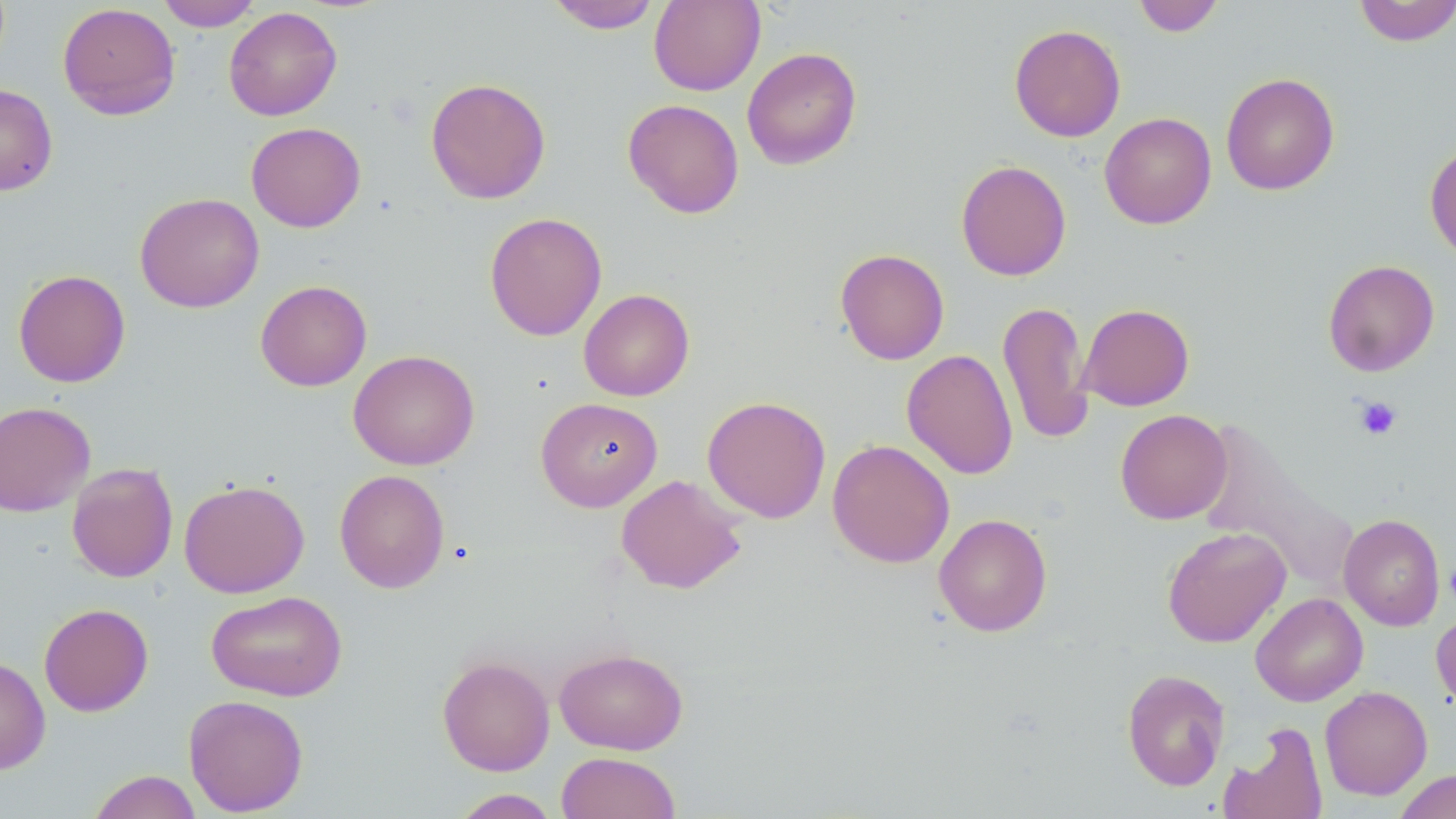

Summary:
  - Coordinate format: approximate bounding boxes as (x1, y1, x2, y2) in pixels
  - Uninfected red blood cell locations: (547, 0, 661, 34), (649, 0, 765, 96), (1133, 0, 1225, 37), (157, 1, 262, 31), (1352, 1, 1456, 46), (57, 3, 181, 120), (224, 6, 342, 121), (1008, 24, 1126, 142), (742, 47, 862, 170), (1221, 72, 1340, 196), (425, 77, 551, 204), (0, 83, 58, 196), (623, 99, 744, 218), (1100, 112, 1216, 229), (245, 122, 366, 232), (1424, 141, 1456, 263), (955, 159, 1071, 281), (134, 192, 264, 313), (484, 212, 607, 341), (835, 248, 950, 365), (1323, 259, 1440, 377), (13, 269, 131, 387), (255, 279, 372, 391), (578, 288, 694, 401), (998, 301, 1093, 445), (1077, 303, 1194, 411), (348, 349, 480, 470), (901, 349, 1018, 479), (702, 395, 831, 523), (536, 397, 663, 512), (0, 401, 96, 517), (1115, 409, 1232, 524), (1195, 421, 1354, 588), (827, 439, 954, 568), (66, 463, 178, 583), (334, 468, 450, 594), (616, 474, 747, 594), (179, 478, 309, 598), (933, 513, 1053, 636), (1338, 513, 1446, 631), (1162, 526, 1291, 647), (206, 590, 347, 701), (1250, 592, 1368, 706), (38, 603, 154, 717), (1432, 608, 1456, 715), (554, 647, 688, 755), (0, 655, 51, 774), (437, 655, 555, 776), (1122, 668, 1230, 791), (1319, 685, 1432, 800), (183, 694, 309, 816), (1220, 722, 1329, 819), (556, 751, 681, 819), (1394, 769, 1456, 819), (87, 770, 203, 819), (450, 789, 560, 818)
  - Platelet locations: (1355, 396, 1402, 440), (1444, 557, 1456, 609)
  - Slide-level diagnosis: negative for blood parasites
  - Modality: optical microscopy
  - Stain: May-Grünwald-Giemsa
  - Preparation: thin blood film
  - Field of view: single
  - Magnification: 1000x
  - Image size: 1456×819 pixels